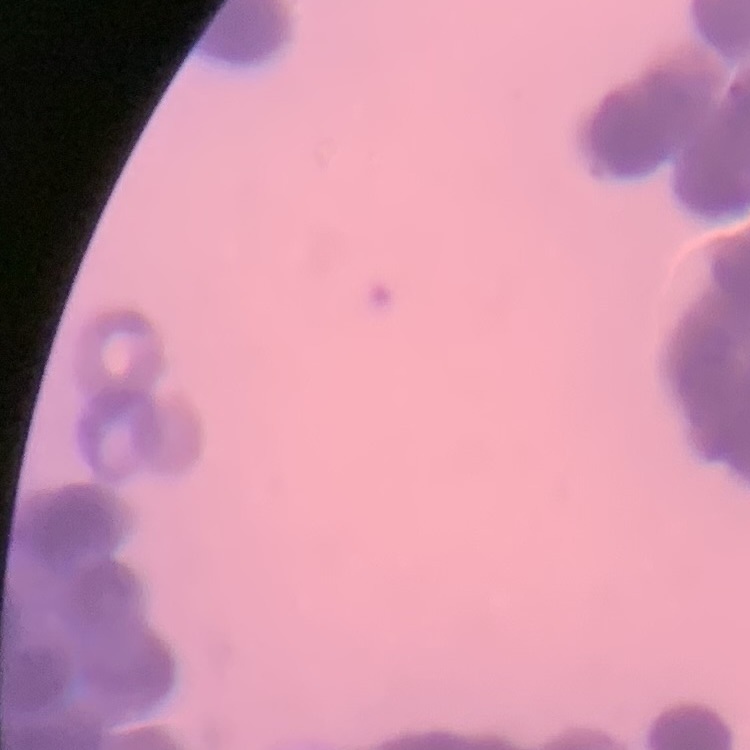

erythrocyte_morphology: rouleaux formation
preparation: thin peripheral smear
stain: Field's or Giemsa
image_type: square crop of a larger photomicrograph